Classify this cell by malaria status.
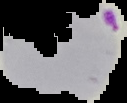

Parasitized.

image_type: segmented cell region on a black background
preparation: thin blood smear
image_size: 127×103 pixels